Report the malaria status of this cell.
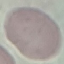
It is uninfected.

stain = Giemsa
preparation = thin blood smear
image type = automatically extracted cell patch, resized to 64 × 64 pixels
capture = smartphone through the microscope eyepiece